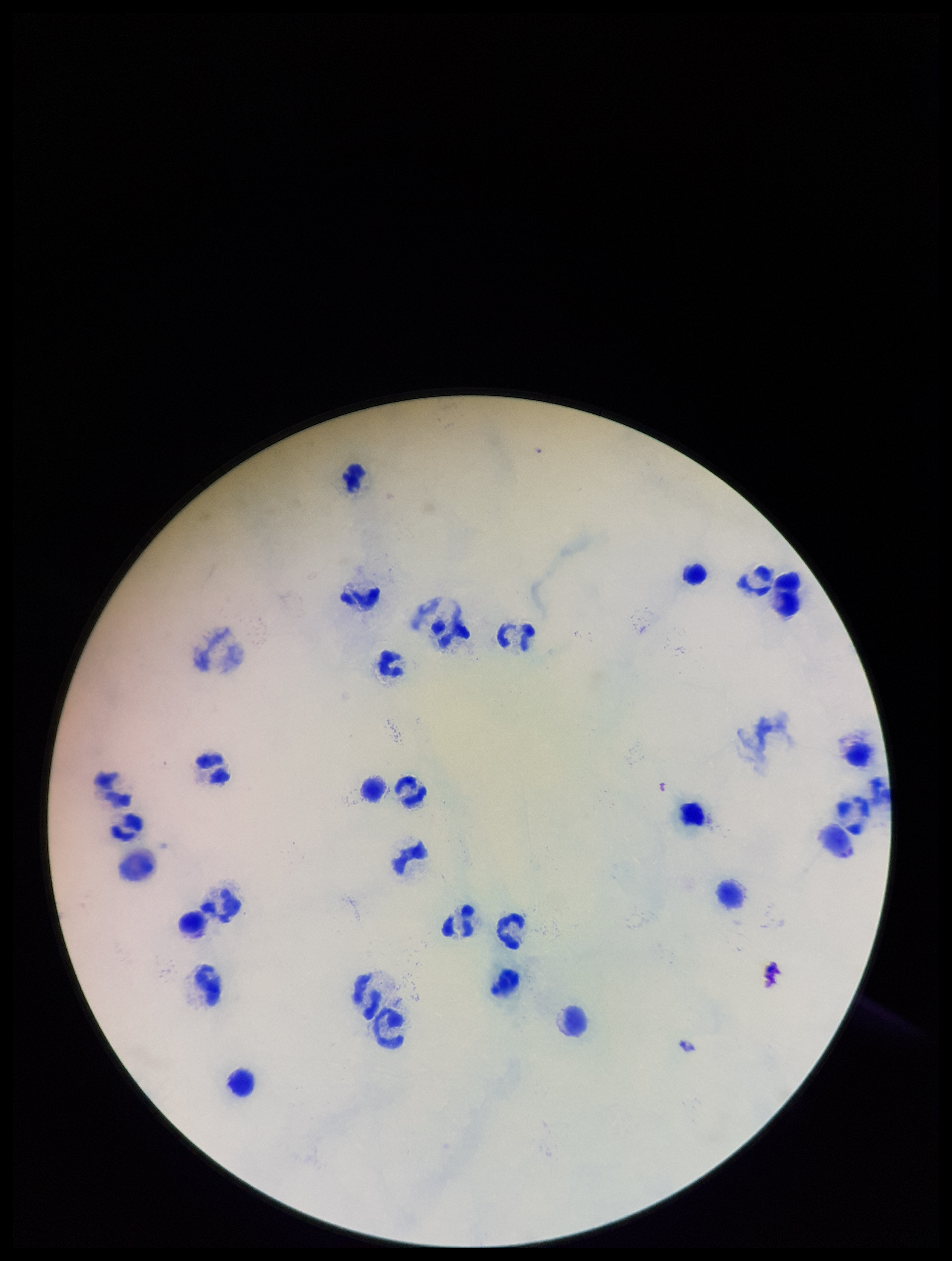

capture = smartphone photograph through the microscope eyepiece
leukocyte count = 31
Plasmodium parasites = none seen
parasite count = 0
field of view = single
patient malaria status = negative
preparation = thick blood smear
image size = 952×1261 pixels
stain = Giemsa